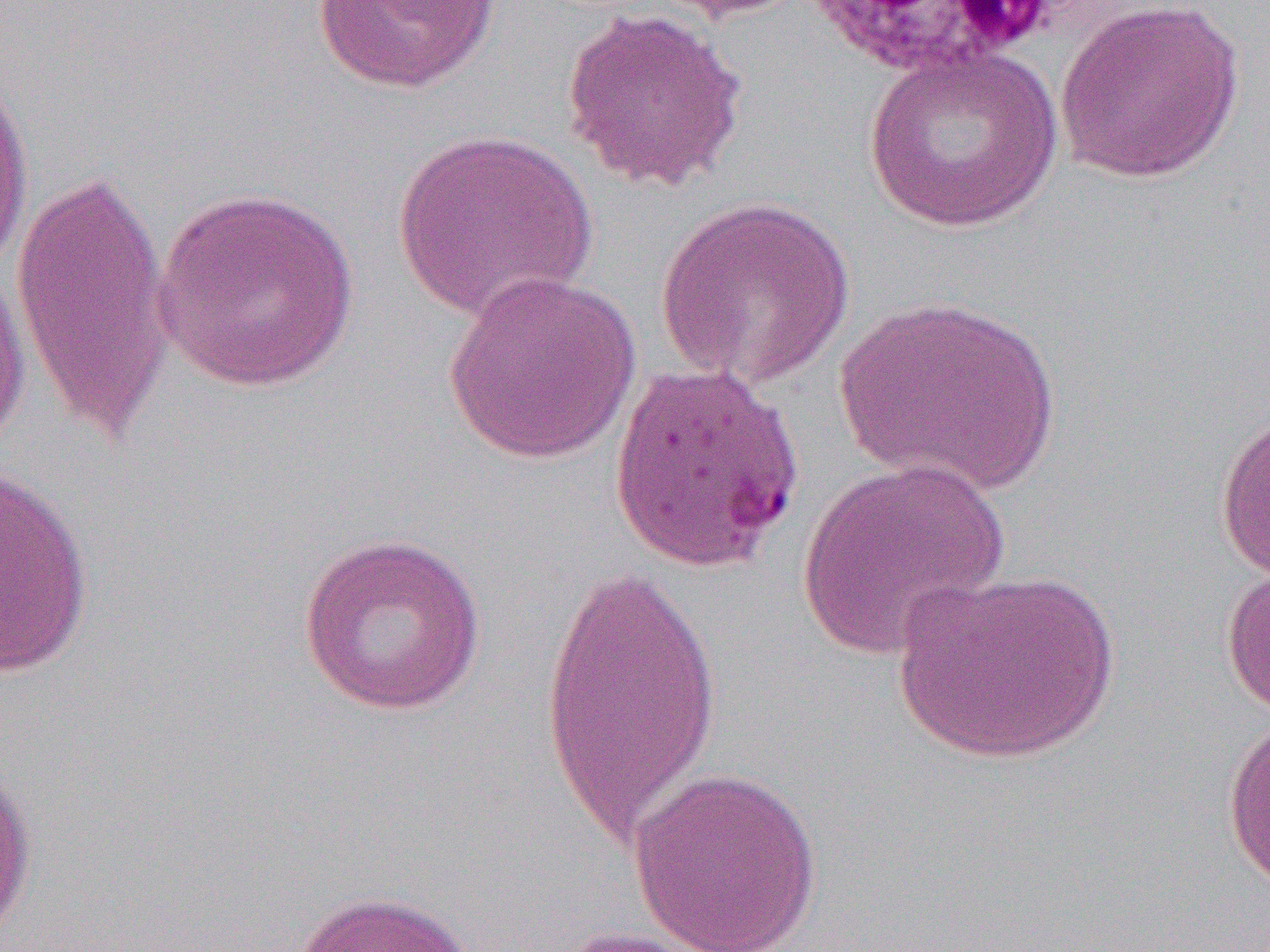

slide-level diagnosis = Plasmodium falciparum
magnification = 1000x
modality = optical microscopy
image size = 1270×952 pixels
preparation = thin blood film
platelet locations = approximate bounding boxes as (x1, y1, x2, y2) in pixels: (950, 1, 1057, 53)
field of view = single
uninfected red blood cell locations = approximate bounding boxes as (x1, y1, x2, y2) in pixels: (311, 0, 504, 95), (644, 0, 810, 25), (1055, 0, 1246, 184), (559, 6, 750, 194), (862, 44, 1063, 233), (0, 64, 35, 282), (389, 129, 600, 323), (9, 164, 175, 447), (152, 185, 363, 394), (655, 195, 853, 390), (0, 264, 32, 461), (442, 270, 645, 465), (835, 295, 1060, 496), (1214, 403, 1270, 585), (796, 457, 1010, 662), (0, 464, 94, 680), (296, 531, 486, 716), (539, 555, 726, 849), (1221, 560, 1270, 722), (893, 568, 1122, 763), (1221, 709, 1270, 892), (0, 753, 39, 945), (626, 766, 824, 952), (288, 889, 479, 952), (544, 925, 725, 952)